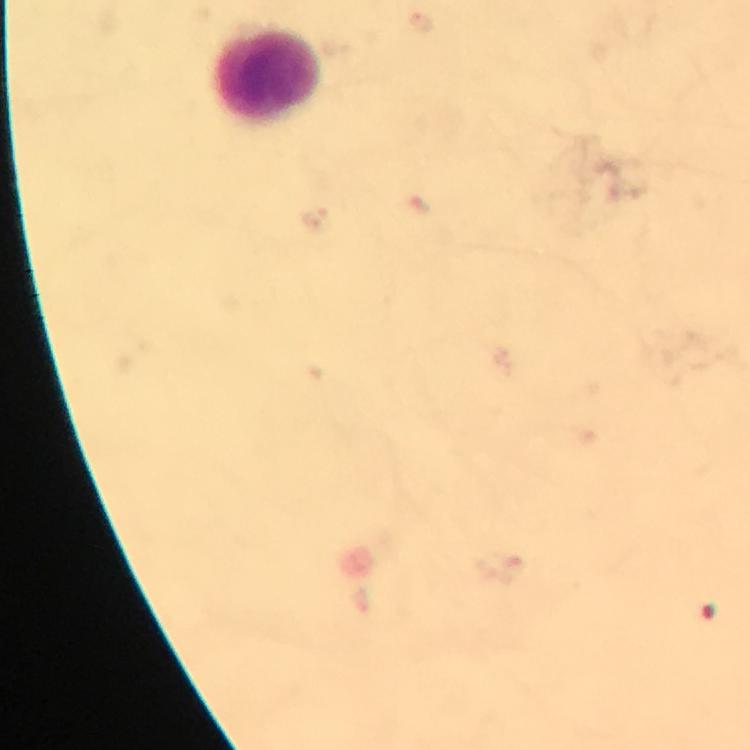

leukocyte locations = approximate centers as [x, y] in pixels: [270, 71]
stain = Giemsa
capture = smartphone photograph through a microscope
malaria parasites = none seen
context = from a malaria diagnostic workup
magnification = 100x
immersion oil = applied
cropped from = a single field of view
image size = 750×750 pixels
preparation = thick blood film